Describe the morphology of the erythrocytes.
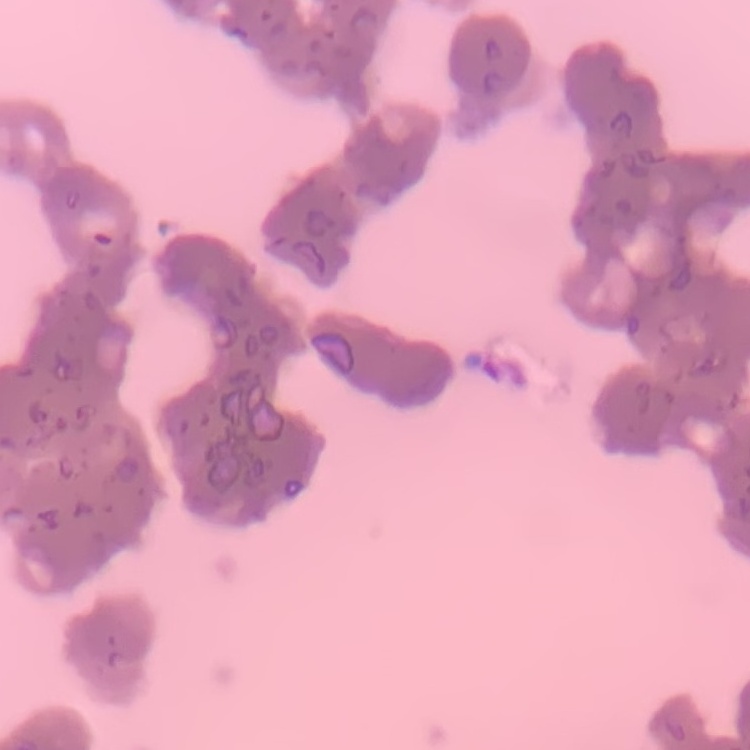

They show rouleaux formation.

Thin blood film. Stained with either Field's or Giemsa. Square crop of a larger photomicrograph.